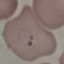
malaria status = parasitized
image type = automatically extracted cell patch, resized to 64 × 64 pixels
stain = Giemsa
preparation = thin blood film
capture = smartphone camera at the microscope eyepiece